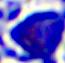

Summary:
  - Identification: leukocyte
  - Magnification: 400x
  - Modality: micrograph